Locate every blood parasite and identify its species.
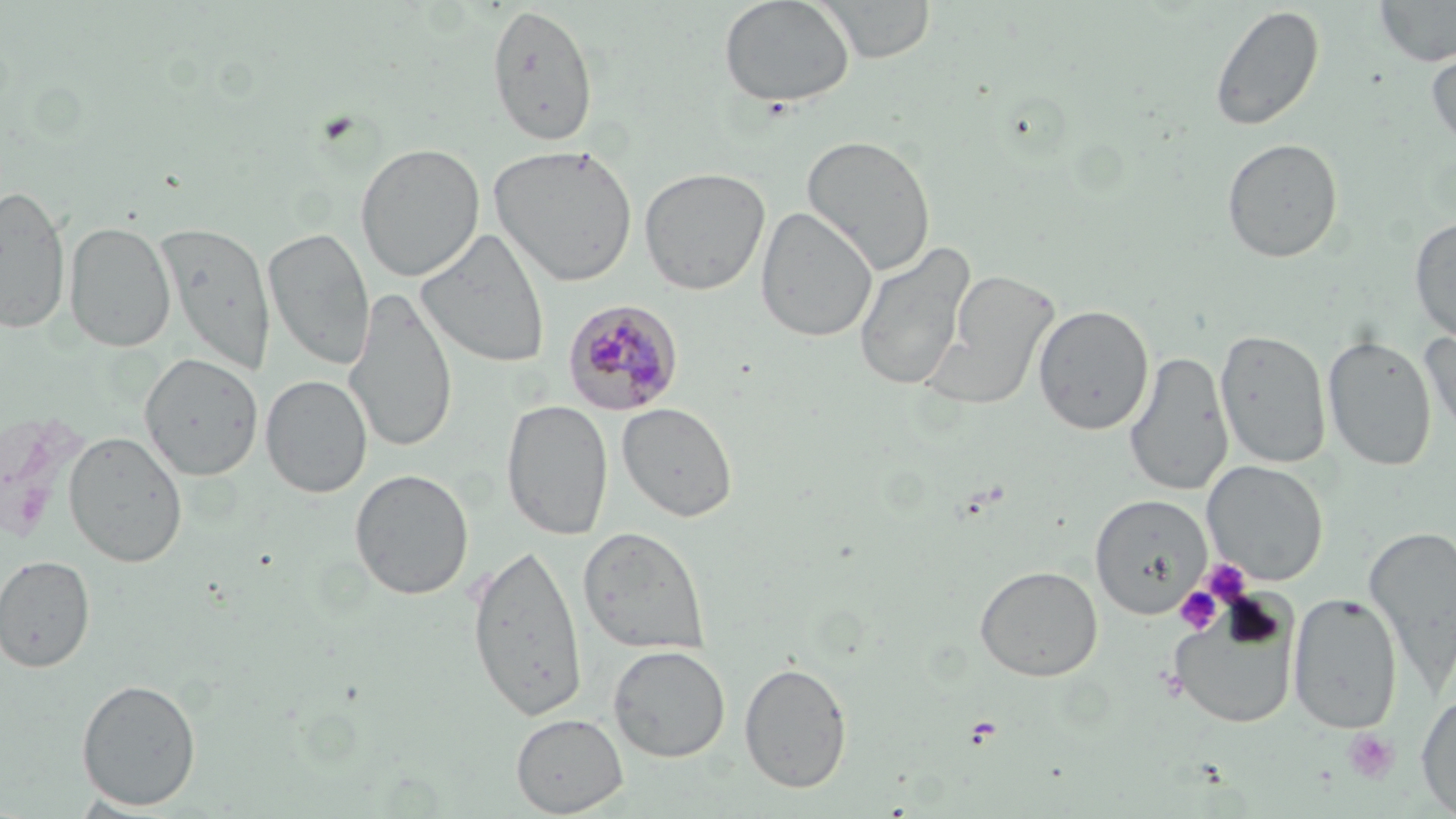

Approximate bounding boxes as (x1,y1)-(x2,y2) corner pairs in pixels.
Plasmodium malariae-infected red blood cells: (563,299)-(685,416).
No Plasmodium falciparum, Plasmodium ovale, Plasmodium vivax, Babesia divergens, or Trypanosoma brucei observed.

slide-level diagnosis = Plasmodium malariae
stain = May-Grünwald-Giemsa
platelet locations = approximate bounding boxes as (x1,y1)-(x2,y2) corner pairs in pixels: (314,110)-(362,147), (1200,559)-(1252,606), (1175,586)-(1222,633), (964,716)-(1004,748), (1341,728)-(1399,784)
preparation = thin blood smear
field of view = single
modality = optical microscopy
image size = 1456×819 pixels
magnification = 1000x
uninfected red blood cell locations = approximate bounding boxes as (x1,y1)-(x2,y2) corner pairs in pixels: (717,0)-(855,109), (817,0)-(937,63), (1373,0)-(1456,67), (486,4)-(599,148), (1209,4)-(1326,132), (1425,45)-(1456,154), (801,134)-(936,276), (1221,138)-(1344,263), (355,143)-(485,282), (488,143)-(638,287), (639,167)-(771,295), (0,184)-(72,336), (756,206)-(877,343), (1409,216)-(1456,344), (64,220)-(177,352), (155,221)-(276,374), (263,227)-(375,371), (416,228)-(551,369), (853,240)-(976,393), (924,268)-(1061,410), (345,288)-(457,455), (1033,304)-(1154,435), (1419,327)-(1456,446), (1214,328)-(1331,469), (1322,335)-(1437,472), (1123,351)-(1233,497), (139,352)-(263,480), (260,375)-(372,498), (502,398)-(614,541), (617,401)-(737,522), (0,411)-(91,547), (63,430)-(187,567), (1202,460)-(1329,585), (349,469)-(474,600), (1090,494)-(1213,617), (578,525)-(711,656), (1363,525)-(1456,694), (466,541)-(588,723), (0,555)-(96,672), (975,565)-(1102,681), (1287,592)-(1402,733), (1167,600)-(1300,729), (608,645)-(731,763), (739,661)-(853,792), (76,678)-(202,811), (1415,690)-(1456,817), (511,713)-(628,817)